Identify the cell.
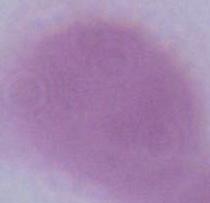

An erythrocyte.

Summary:
  - Magnification: 1000x
  - Modality: micrograph